Report the malaria status of this cell.
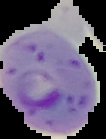
Parasitized.

{
  "image_size": "106×139 pixels",
  "preparation": "thin blood film",
  "image_type": "segmented cell region on a black background"
}